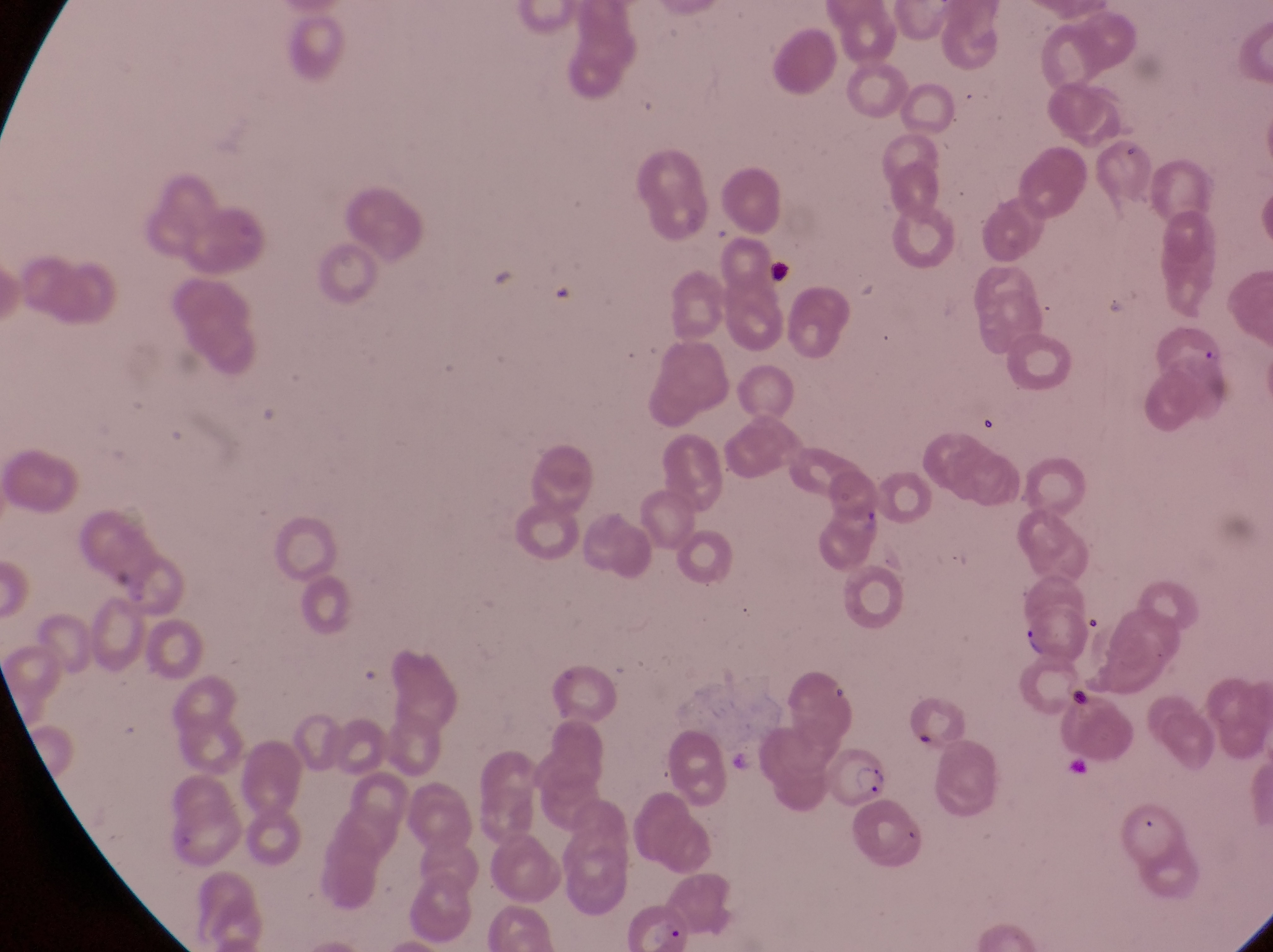
{
  "magnification": "1000x",
  "capture": "smartphone photograph through the eyepiece of an Olympus CX-23 microscope",
  "country": "Uganda",
  "image_size": "1273×952 pixels",
  "leukocyte_locations": "approximate bounding boxes as {left, top, right, bottom} in pixels: {762, 253, 794, 292}",
  "field_of_view": "single",
  "preparation": "thin blood film",
  "parasitised_red_blood_cell_locations": "approximate bounding boxes as {left, top, right, bottom} in pixels: {1021, 606, 1100, 666}, {822, 744, 891, 809}"
}